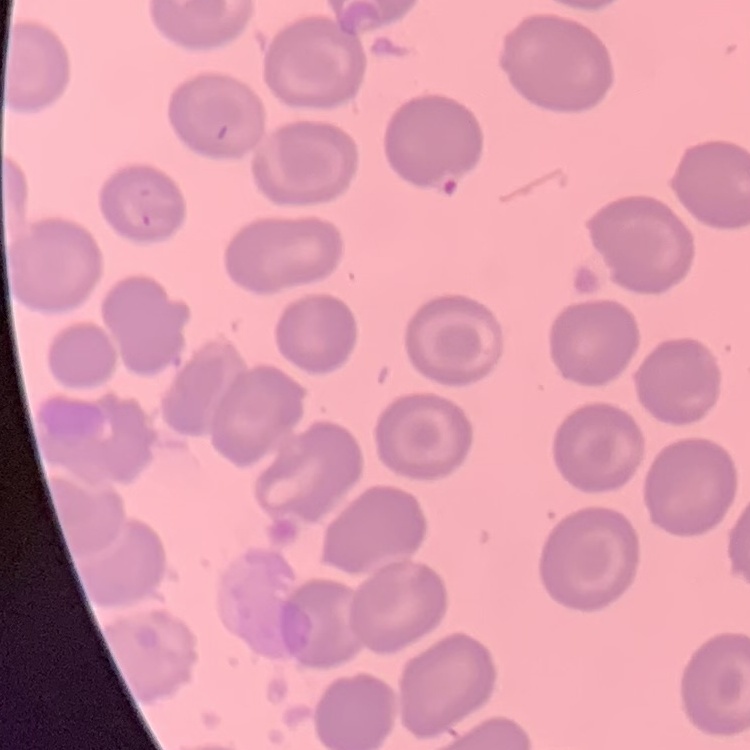

red_blood_cell_morphology: no rouleaux formation
stain: Field's or Giemsa
image_type: square crop of a larger photomicrograph
preparation: thin blood smear